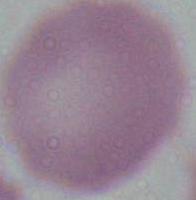
Summary:
  - Identification: red blood cell
  - Magnification: 1000x
  - Modality: micrograph